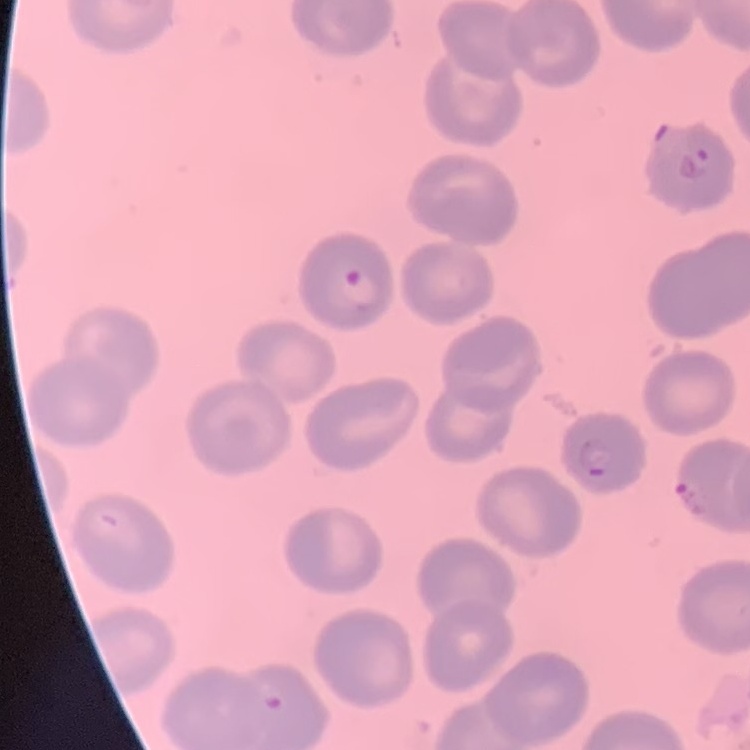

Summary:
  - Red blood cell morphology: no rouleaux formation
  - Image type: one tile cut from a larger photomicrograph
  - Preparation: thin peripheral smear
  - Stain: Field's or Giemsa